Assess this cell for malaria.
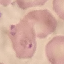
Parasitized.

Summary:
  - Preparation: thin blood film
  - Stain: Giemsa
  - Image type: cell patch, automatically extracted from a larger field of view and resized to 64 × 64 pixels
  - Capture: smartphone camera at the microscope eyepiece